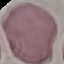
Result: no malaria parasites seen. Cell patch, automatically extracted from a larger field of view and resized to 64 × 64 pixels. Giemsa-stained preparation. Photographed with a smartphone camera at the microscope eyepiece. Thin blood smear.